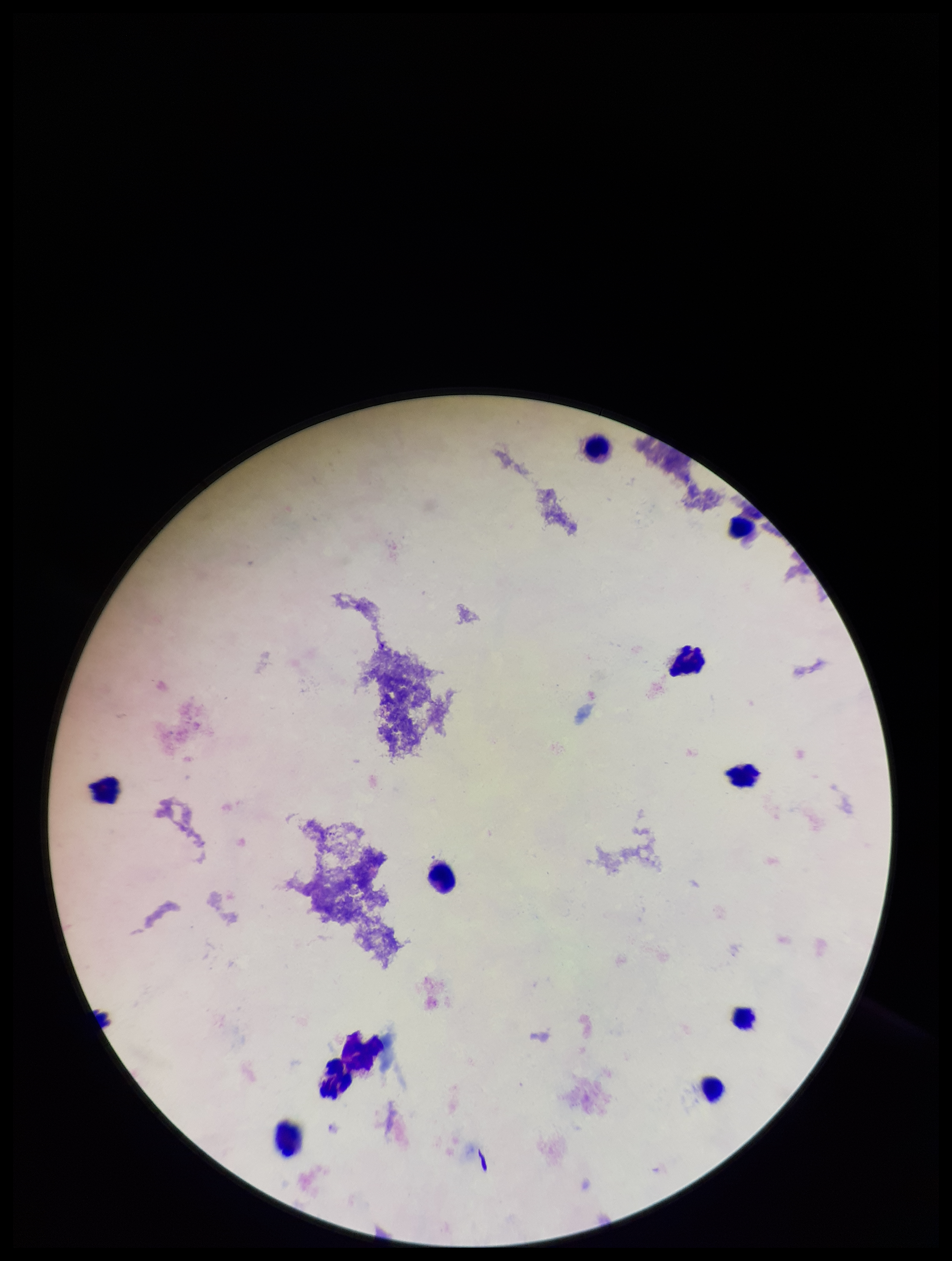

Summary:
  - Plasmodium parasites: none seen
  - Field of view: single
  - Parasite count: 0
  - Preparation: thick
  - Capture: smartphone photograph through the microscope eyepiece
  - Image size: 952×1261 pixels
  - Stain: Giemsa
  - Patient malaria status: negative
  - Leukocyte count: 11